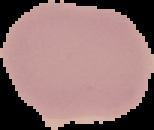 Result: negative for Plasmodium parasites. Image is 154×130 pixels. Segmented cell region on a black background. From a thin blood film.